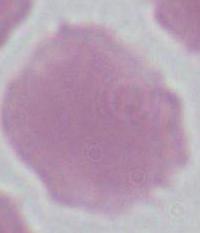
Photomicrograph. Captured at 1000x magnification. An erythrocyte is seen.